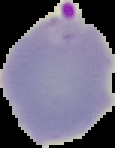

malaria_status: parasitized
preparation: thin blood smear
image_size: 115×148 pixels
image_type: segmented cell region on a black background